State which parasite is depicted.
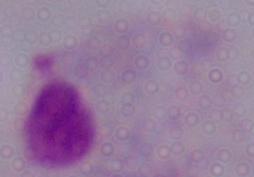

This is a trichomonad.

modality = photomicrograph
magnification = 1000x